Classify this cell by malaria status.
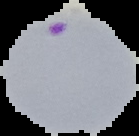

Parasitized.

Summary:
  - Preparation: thin blood smear
  - Image type: segmented cell region on a black background
  - Image size: 139×136 pixels